Assess this cell for malaria.
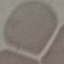
Uninfected.

Summary:
  - Stain: Giemsa
  - Image type: automatically extracted cell patch, resized to 64 × 64 pixels
  - Preparation: thin blood film
  - Capture: smartphone camera at the microscope eyepiece